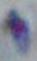

identification = Toxoplasma gondii
modality = micrograph
magnification = 1000x